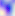
{
  "modality": "photomicrograph",
  "identification": "Toxoplasma gondii",
  "magnification": "400x"
}